Classify this cell by malaria status.
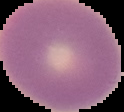
It is uninfected.

Image is 124×112 pixels. The area outside the segmented cell region is set to black. From a thin blood film.